Report the malaria status of this cell.
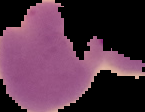

Parasitized.

Summary:
  - Image size: 145×112 pixels
  - Preparation: thin blood smear
  - Image type: cell region segmented out of the field of view; surrounding area masked to black